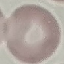
Result: no malaria parasites seen. Thin smear of blood. Acquired by smartphone through the microscope eyepiece. Giemsa stain. Cell patch, automatically extracted from a larger field of view and resized to 64 × 64 pixels.